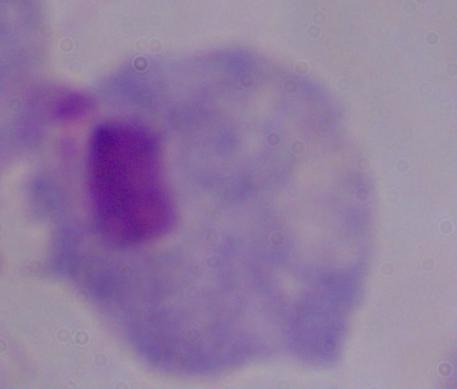
identification: trichomonad
magnification: 1000x
modality: micrograph